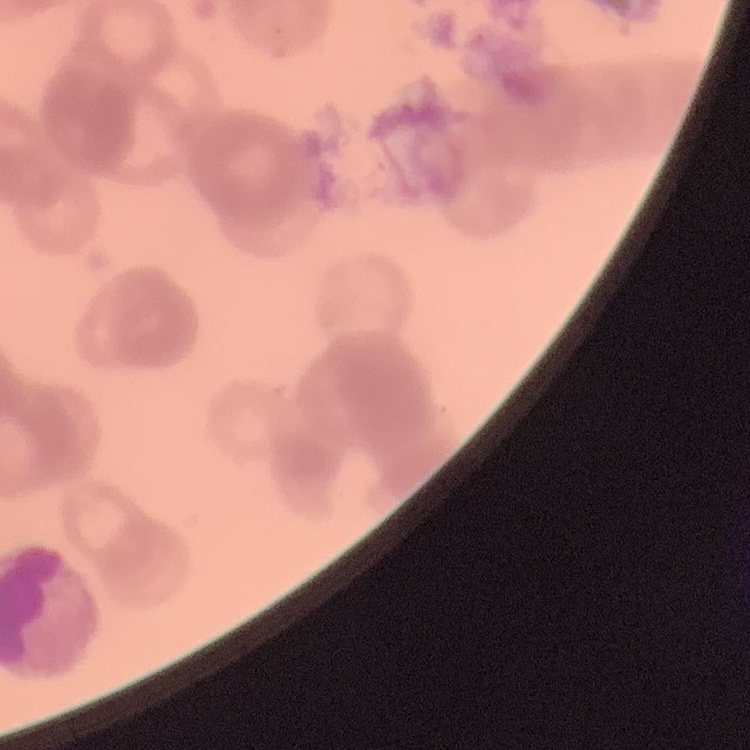

The erythrocytes show rouleaux formation. Square crop of a larger photomicrograph. Thin blood smear. Stained with either Field's or Giemsa.